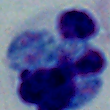 A leukocyte is shown. Captured at 1000x magnification. Photomicrograph.